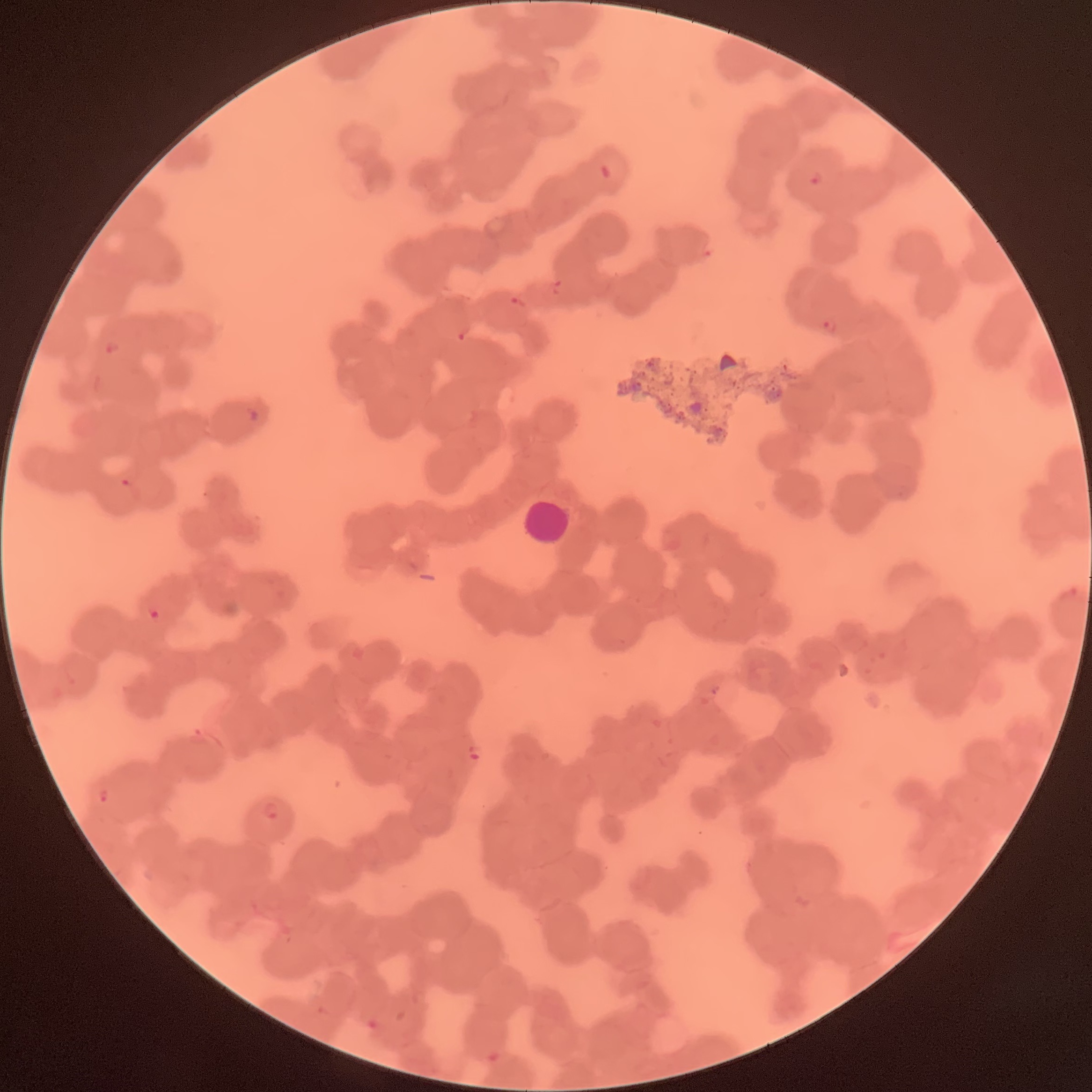
modality: light microscopy
plasmodium_parasite_locations: 'approximate bounding boxes as (x1,y1)-(x2,y2) corner pairs in pixels: (809,169)-(824,186), (512,295)-(528,308), (823,316)-(838,334), (457,323)-(471,342), (104,340)-(119,356), (249,406)-(261,423), (120,476)-(139,501), (899,486)-(912,500), (148,608)-(162,622), (708,686)-(718,695), (192,725)-(209,746), (466,749)-(480,760), (96,787)-(109,804), (260,801)-(282,820)'
red_blood_cell_morphology: rouleaux formation
white_blood_cell_locations: 'approximate bounding boxes as (x1,y1)-(x2,y2) corner pairs in pixels: (521,497)-(571,547)'
image_size: 1092×1092 pixels
preparation: thin blood film